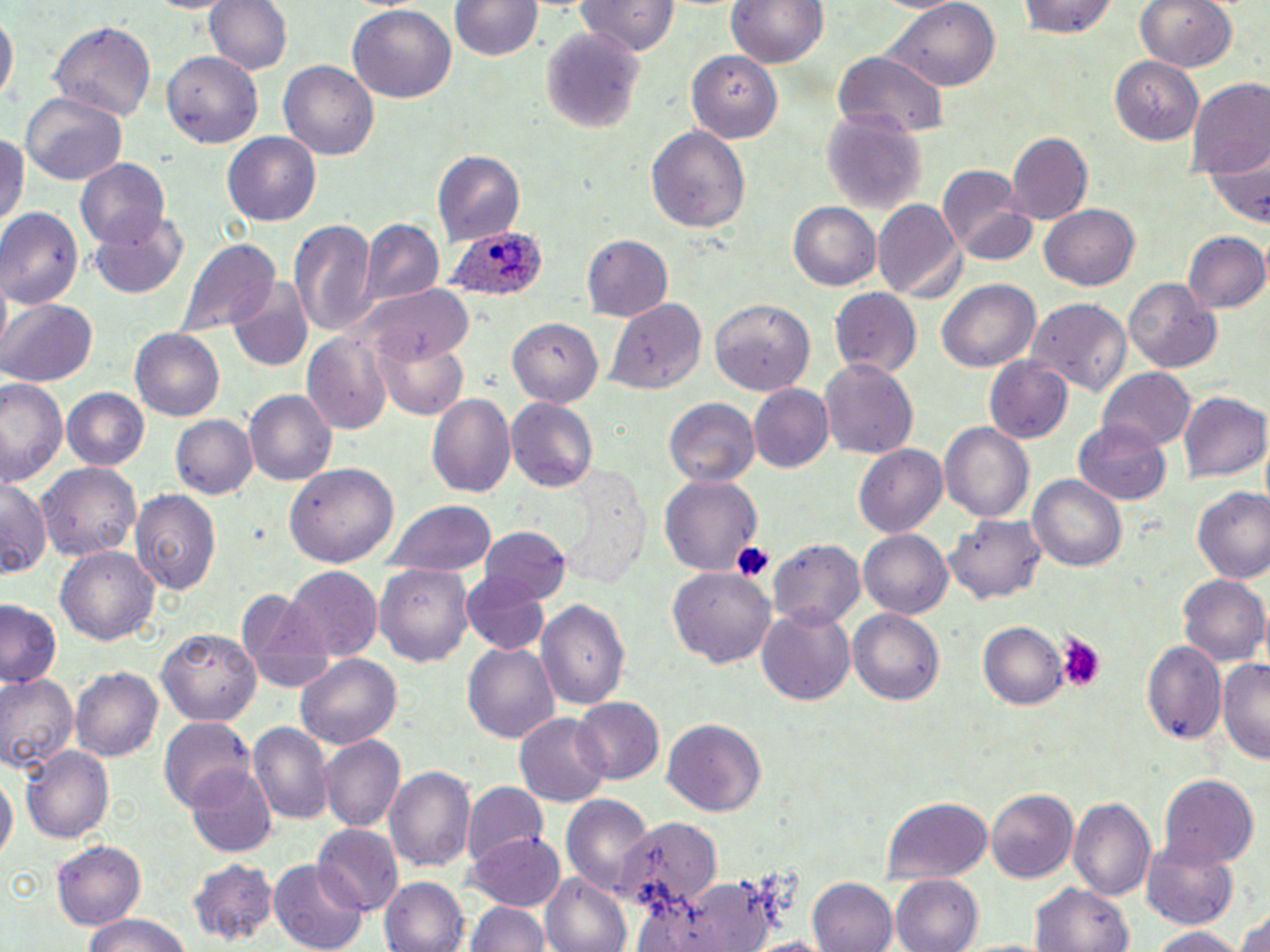
Summary:
  - Coordinate format: approximate bounding boxes as [x1, y1, x2, y2] in pixels
  - Plasmodium ovale-infected red blood cell locations: [444, 231, 548, 302]
  - Uninfected red blood cell locations: [203, 0, 291, 78], [575, 0, 681, 57], [728, 0, 826, 69], [1018, 0, 1120, 40], [1135, 0, 1238, 72], [452, 1, 540, 62], [886, 3, 1000, 93], [347, 4, 456, 103], [1, 11, 15, 110], [51, 21, 157, 125], [542, 31, 644, 130], [686, 49, 784, 143], [160, 51, 263, 148], [835, 54, 948, 138], [1110, 54, 1207, 143], [279, 59, 379, 159], [1187, 78, 1270, 175], [21, 91, 127, 182], [820, 112, 927, 215], [645, 124, 750, 233], [0, 129, 28, 232], [225, 132, 322, 225], [1006, 132, 1093, 222], [434, 151, 525, 245], [74, 159, 169, 250], [1200, 161, 1269, 227], [939, 164, 1036, 265], [871, 199, 962, 303], [787, 201, 880, 291], [1039, 204, 1139, 290], [0, 209, 83, 310], [90, 214, 188, 298], [290, 219, 377, 336], [362, 219, 445, 309], [1182, 230, 1269, 314], [580, 234, 671, 322], [179, 238, 280, 336], [1122, 277, 1221, 373], [937, 280, 1039, 374], [351, 284, 475, 370], [230, 286, 314, 373], [831, 290, 921, 378], [606, 296, 705, 393], [1, 298, 99, 387], [708, 298, 816, 397], [1025, 299, 1130, 397], [505, 316, 602, 405], [133, 328, 226, 421], [303, 330, 394, 432], [374, 332, 471, 418], [819, 357, 919, 461], [984, 357, 1073, 444], [1099, 367, 1195, 452], [0, 376, 66, 484], [750, 386, 833, 473], [60, 387, 149, 470], [245, 390, 336, 485], [427, 391, 515, 498], [1180, 392, 1268, 484], [664, 396, 759, 487], [506, 398, 597, 489], [170, 412, 258, 499], [1074, 417, 1172, 505], [941, 423, 1033, 524], [851, 444, 947, 535], [283, 461, 398, 568], [38, 462, 142, 563], [561, 476, 648, 588], [660, 476, 761, 575], [1030, 477, 1126, 571], [0, 480, 52, 579], [1190, 488, 1270, 584], [133, 490, 221, 597], [388, 501, 497, 576], [945, 515, 1045, 604], [479, 526, 571, 605], [860, 529, 951, 617], [770, 540, 865, 632], [55, 545, 160, 648], [378, 563, 473, 668], [670, 568, 776, 669], [286, 569, 383, 660], [460, 571, 556, 656], [1178, 575, 1267, 666], [237, 586, 332, 690], [536, 598, 632, 709], [1, 604, 59, 686], [757, 604, 856, 707], [848, 610, 943, 705], [979, 620, 1068, 708], [157, 627, 262, 724], [1143, 640, 1227, 746], [464, 642, 559, 745], [295, 651, 405, 750], [1219, 656, 1270, 763], [71, 664, 163, 759], [0, 673, 78, 772], [571, 698, 664, 787], [514, 712, 611, 806], [160, 717, 257, 807], [661, 718, 766, 817], [249, 720, 336, 827], [319, 736, 402, 832], [20, 746, 117, 842], [186, 763, 277, 855], [388, 765, 476, 873], [0, 770, 14, 870], [1158, 775, 1258, 868], [462, 781, 548, 872], [986, 788, 1079, 884], [560, 793, 654, 899], [880, 797, 992, 882], [1071, 799, 1156, 899], [614, 817, 717, 915], [313, 825, 403, 915], [471, 833, 565, 912], [1143, 838, 1241, 930], [53, 841, 146, 929], [187, 857, 279, 944], [269, 861, 366, 952], [541, 874, 630, 952], [892, 876, 983, 952], [381, 878, 468, 952], [807, 878, 898, 952], [1035, 883, 1135, 952], [467, 900, 550, 952], [1237, 908, 1270, 952], [76, 916, 196, 952], [1144, 926, 1250, 951]
  - Platelet locations: [730, 539, 775, 587], [1057, 634, 1103, 690]
  - Slide-level diagnosis: Plasmodium ovale
  - Magnification: 1000x
  - Modality: optical microscopy
  - Image size: 1270×952 pixels
  - Preparation: thin blood film
  - Field of view: one of a larger specimen
  - Stain: May-Grünwald-Giemsa